Classify this cell by malaria status.
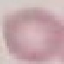
Uninfected.

Automatically extracted cell patch, resized to 64 × 64 pixels. Giemsa-stained preparation. Photographed with a smartphone camera at the microscope eyepiece. Thin blood smear.